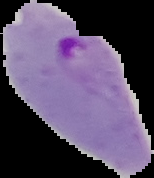

image type = segmented cell region on a black background
image size = 154×178 pixels
preparation = thin blood film
result = Plasmodium parasites identified